Assess this cell for malaria.
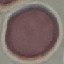

Uninfected.

preparation = thin blood film
stain = Giemsa
image type = automatically extracted cell patch, resized to 64 × 64 pixels
capture = smartphone camera at the microscope eyepiece